Classify this cell by malaria status.
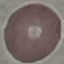

It is uninfected.

Summary:
  - Image type: automatically extracted cell patch, resized to 64 × 64 pixels
  - Preparation: thin blood smear
  - Capture: smartphone camera at the microscope eyepiece
  - Stain: Giemsa